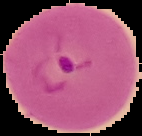 Image is 142×136 pixels. Segmented cell region on a black background. From a thin blood smear. Malaria status: parasitized.